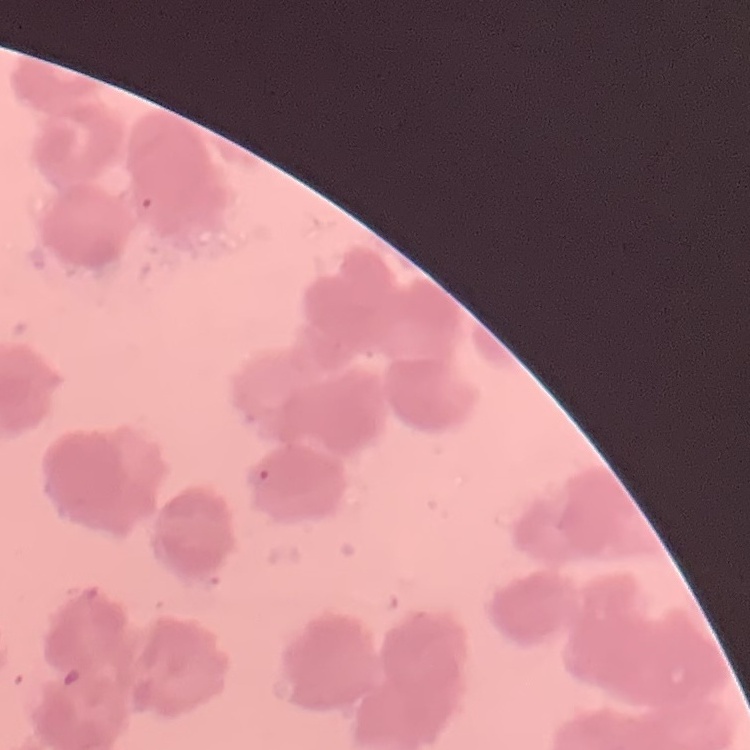 The erythrocytes exhibit rouleaux formation. Square crop of a larger photomicrograph. Field's or Giemsa stain. Thin blood film.